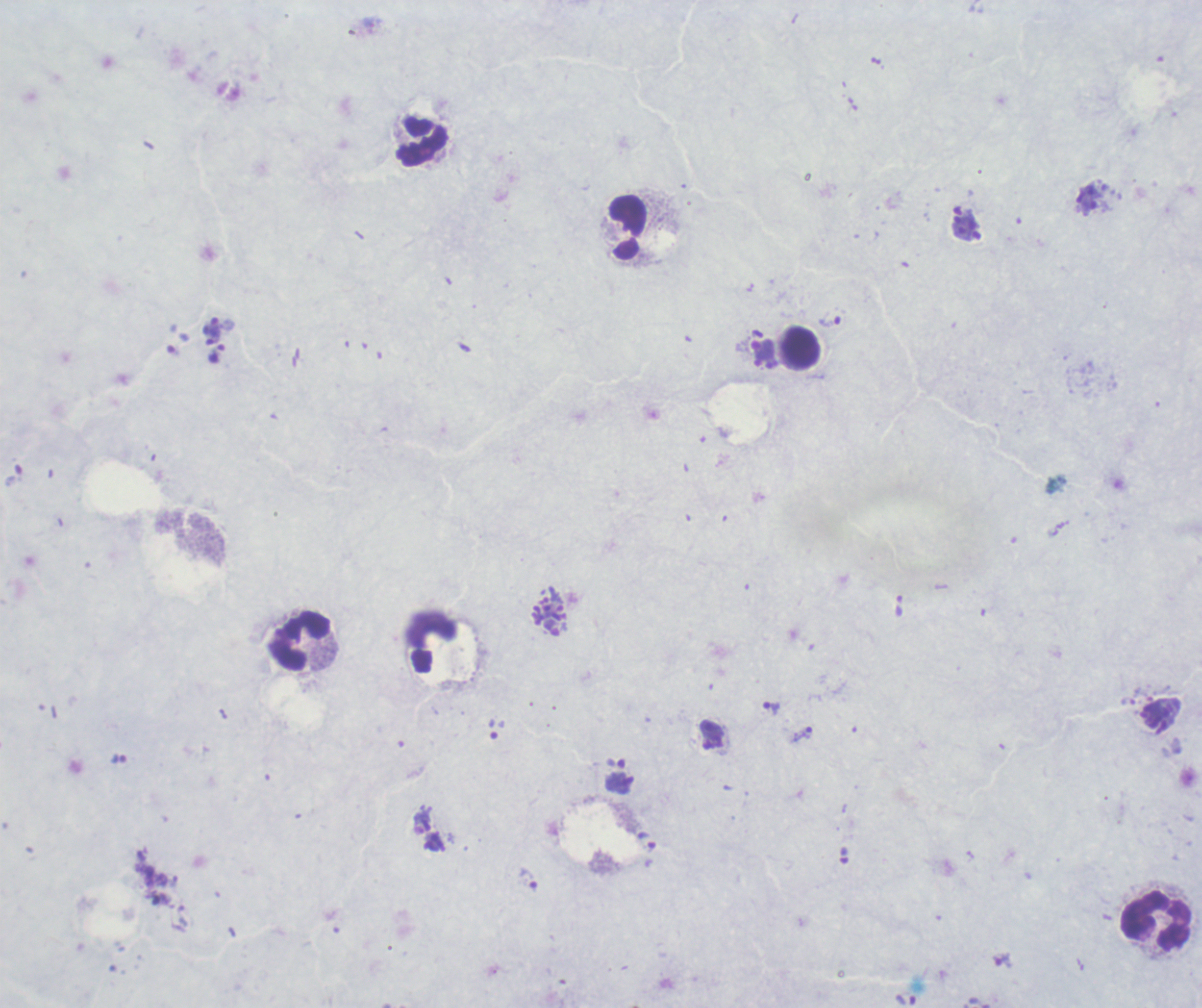
Approximate centers as {x, y} in pixels.
Summary:
  - Schizont locations: {966, 224}, {764, 354}
  - Trophozoite locations: {830, 322}, {214, 328}, {217, 353}, {550, 617}, {1128, 701}, {771, 707}, {804, 734}, {119, 759}, {529, 879}, {1003, 961}
  - Leukocyte locations: {422, 141}, {628, 227}, {800, 348}, {299, 641}, {1156, 921}
  - Life-cycle stages observed: trophozoite, schizont
  - Magnification: 100x
  - Context: previously used in a real diagnosis
  - Stain: Romanowsky
  - Field of view: single
  - Result: malaria parasites detected
  - Preparation: thick blood film
  - Background quality: poor
  - Image size: 1202×1008 pixels